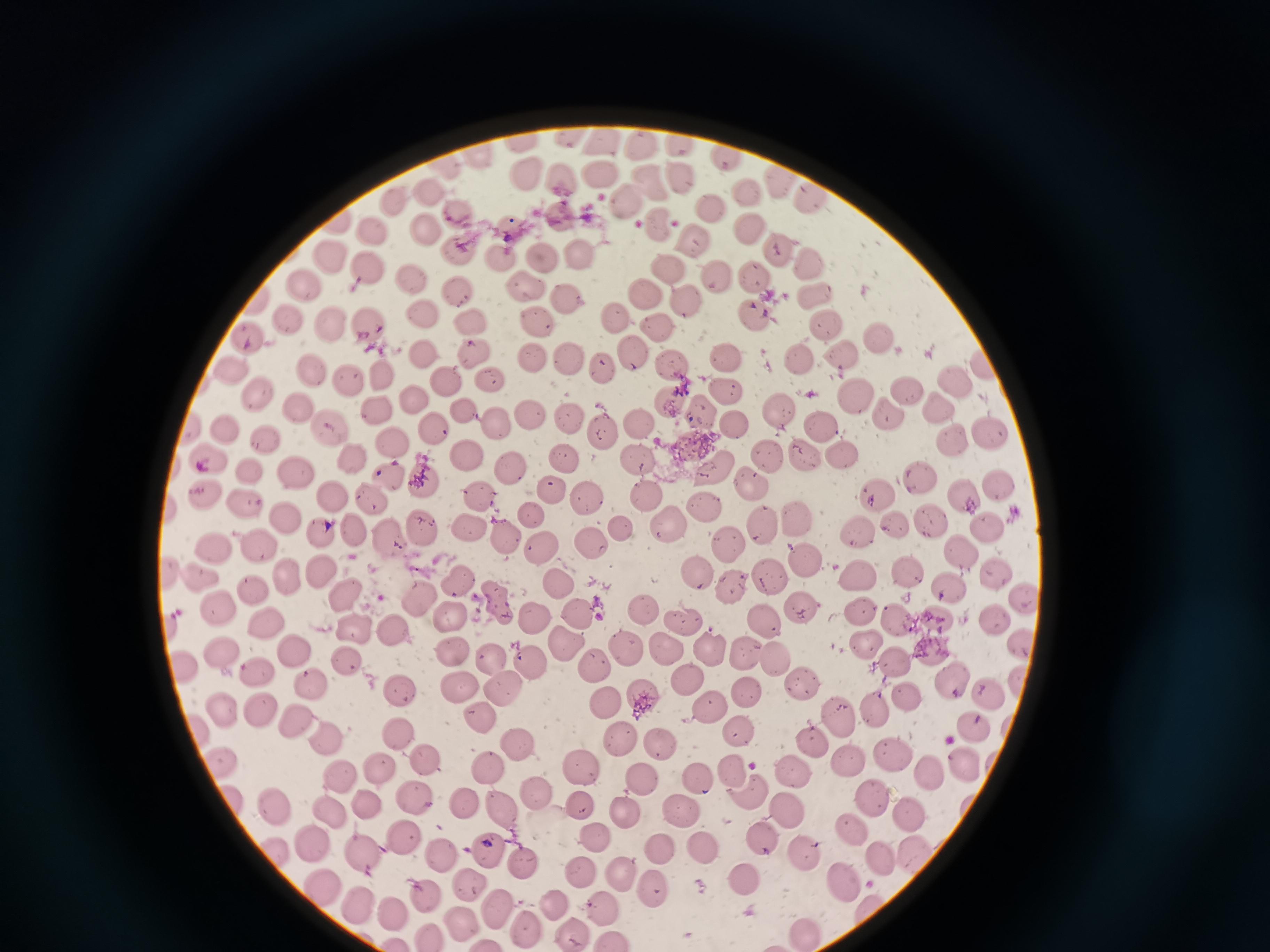

Approximate centers as [x, y] in pixels. Cell locations: [566, 137], [604, 139], [523, 141], [641, 143], [678, 144], [477, 155], [724, 158], [525, 175], [598, 175], [564, 176], [680, 176], [647, 181], [778, 183], [745, 192], [431, 193], [813, 196], [629, 199], [396, 204], [710, 204], [457, 207], [562, 213], [660, 224], [428, 227], [747, 227], [373, 231], [694, 238], [776, 249], [462, 252], [542, 252], [577, 254], [337, 255], [496, 256], [810, 262], [365, 266], [670, 270], [410, 276], [752, 276], [718, 278], [309, 284], [529, 285], [460, 289], [568, 293], [643, 293], [814, 300], [685, 301], [423, 312], [754, 312], [538, 315], [613, 316], [288, 322], [328, 323], [470, 325], [366, 326], [656, 326], [824, 326], [246, 337], [880, 338], [533, 351], [631, 351], [425, 352], [474, 354], [728, 354], [563, 356], [841, 356], [796, 358], [673, 366], [605, 368], [229, 371], [316, 371], [380, 373], [442, 377], [349, 378], [490, 380], [955, 381], [908, 387], [258, 391], [725, 391], [858, 392], [418, 398], [670, 404], [298, 408], [780, 408], [887, 409], [940, 410], [378, 411], [464, 411], [704, 411], [528, 413], [569, 415], [495, 422], [635, 422], [736, 424], [818, 424], [332, 427], [224, 428], [603, 429], [436, 432], [987, 432], [953, 437], [393, 439], [271, 440], [842, 449], [802, 453], [213, 455], [466, 456], [566, 457], [355, 458], [636, 458], [766, 459], [510, 468], [253, 469], [714, 469], [295, 472], [919, 473], [387, 477], [427, 479], [751, 480], [1000, 486], [550, 489], [205, 490], [873, 490], [333, 493], [647, 495], [371, 496], [483, 496], [966, 496], [588, 500], [247, 502], [706, 509], [532, 513], [928, 514], [286, 517], [794, 517], [891, 522], [665, 523], [764, 523], [986, 523], [351, 527], [425, 528], [466, 528], [623, 528], [326, 530], [858, 531], [391, 535], [509, 538], [591, 542], [726, 542], [261, 545], [215, 546], [540, 546], [959, 546], [804, 555], [321, 569], [914, 569], [994, 569], [198, 573], [770, 573], [698, 574], [863, 575], [288, 576], [556, 580], [459, 582], [953, 583], [731, 585], [255, 592], [346, 594], [418, 599], [1023, 599], [798, 601], [495, 603], [217, 607], [860, 609], [642, 610], [579, 611], [897, 615], [446, 616], [535, 617], [995, 617], [681, 619], [933, 619], [765, 621], [268, 626], [353, 628], [398, 629], [565, 640], [867, 640], [1022, 642], [667, 646], [710, 646], [623, 647], [936, 648], [454, 649], [748, 649], [220, 650], [294, 650], [487, 655], [773, 656], [348, 658], [529, 662], [592, 663], [901, 663], [183, 668], [263, 672], [688, 675], [803, 677], [1022, 677], [955, 679], [315, 681], [458, 684], [505, 687], [990, 687], [749, 689], [401, 690], [644, 695], [902, 695], [608, 699], [223, 705], [261, 707], [713, 708], [873, 711], [478, 713], [835, 719], [291, 723], [398, 729], [743, 732], [973, 732], [329, 738], [815, 739], [623, 742], [658, 742], [518, 745], [891, 755], [847, 758], [429, 759], [220, 762], [381, 766], [486, 767], [959, 767], [580, 768], [931, 769], [732, 771], [695, 773], [345, 774], [796, 774], [642, 778], [747, 790], [537, 794], [414, 797], [873, 799], [371, 801], [464, 803], [499, 803], [581, 803], [333, 806], [273, 808], [628, 809], [680, 809], [786, 813], [911, 815], [851, 826], [596, 833], [401, 834], [762, 839], [315, 840], [702, 844], [489, 845], [662, 846], [363, 850], [805, 851], [443, 855], [914, 855], [523, 856], [876, 858], [582, 871], [628, 874], [745, 878], [847, 878], [323, 883], [467, 883], [659, 886], [424, 891], [361, 901], [552, 902], [603, 903], [494, 907], [391, 908], [459, 918], [525, 926], [808, 927], [574, 932]. Image is 1270×952 pixels. Thin smear of blood. Giemsa-stained preparation. Acquired by smartphone through the microscope eyepiece. Single field of view.